Classify this cell by malaria status.
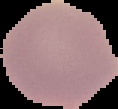

Uninfected.

Segmented cell region on a black background. From a thin blood film. Image is 118×109 pixels.